Assess this cell for malaria.
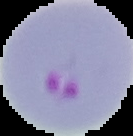

Parasitized.

Segmented cell region on a black background. From a thin blood smear. Image is 133×136 pixels.